Assess this cell for malaria.
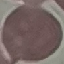

It is uninfected.

Automatically extracted cell patch, resized to 64 × 64 pixels. Thin smear of blood. Photographed with a smartphone camera at the microscope eyepiece. Giemsa-stained preparation.